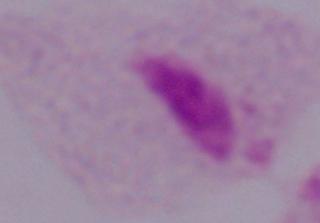

Summary:
  - Identification: trichomonad
  - Modality: micrograph
  - Magnification: 1000x